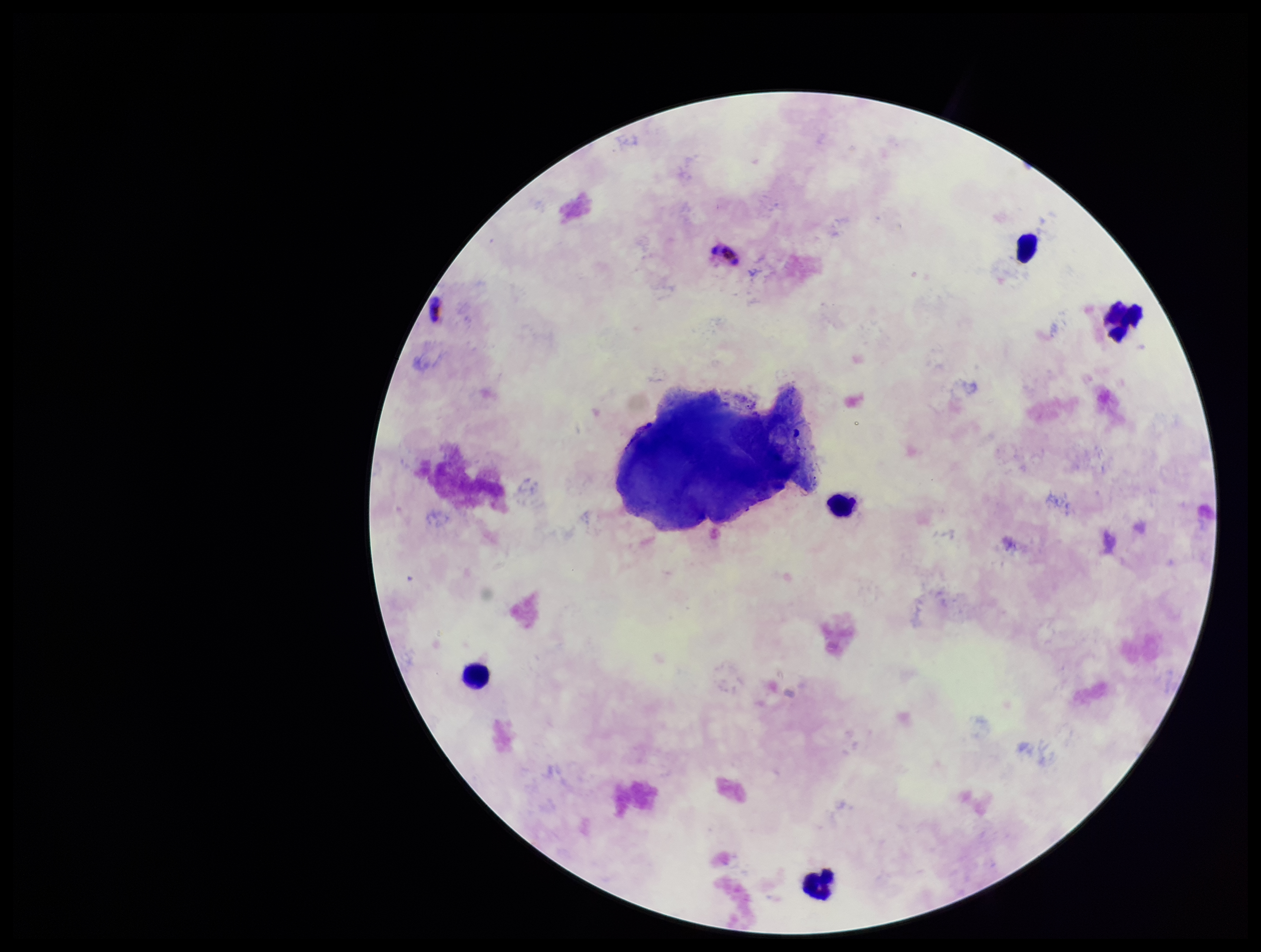
stain = Giemsa
image size = 1261×952 pixels
leukocyte count = 5
patient malaria status = positive
preparation = thick blood smear
species reported for this patient = Plasmodium falciparum
capture = smartphone photograph through the microscope eyepiece
Plasmodium parasites = none detected
parasite count = 0
field of view = one from this slide